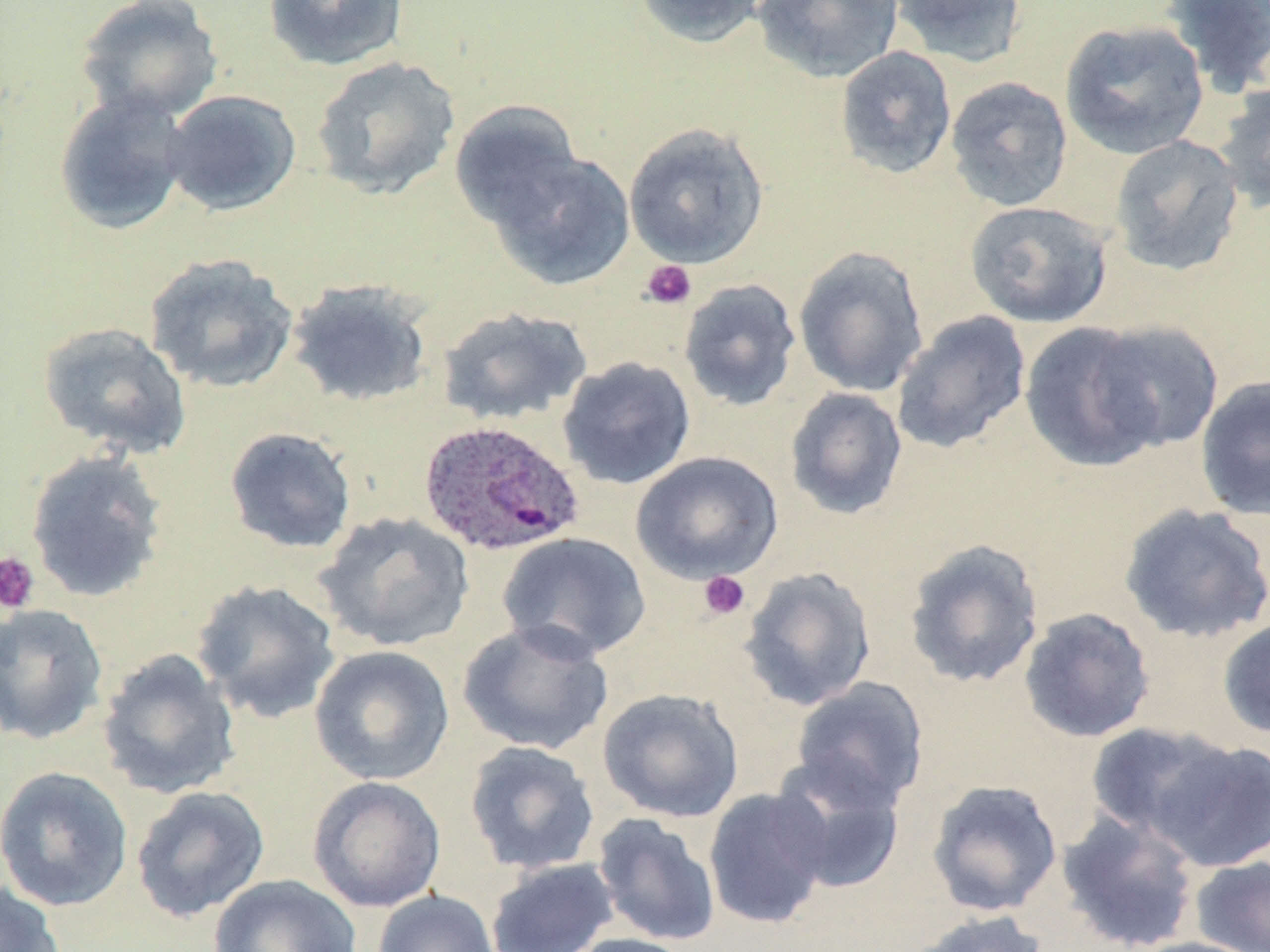
Summary:
  - Coordinate format: approximate bounding boxes as named x1/y1/x2/y2 corners in pixels
  - Uninfected red blood cell locations: (x1=74, y1=0, x2=224, y2=124), (x1=262, y1=0, x2=408, y2=71), (x1=632, y1=0, x2=768, y2=49), (x1=752, y1=0, x2=904, y2=83), (x1=889, y1=0, x2=1028, y2=68), (x1=1161, y1=0, x2=1270, y2=98), (x1=1059, y1=19, x2=1210, y2=160), (x1=834, y1=46, x2=957, y2=179), (x1=311, y1=55, x2=461, y2=200), (x1=944, y1=76, x2=1073, y2=212), (x1=1212, y1=82, x2=1270, y2=214), (x1=161, y1=89, x2=302, y2=216), (x1=53, y1=90, x2=192, y2=236), (x1=448, y1=100, x2=585, y2=233), (x1=623, y1=122, x2=769, y2=268), (x1=1109, y1=135, x2=1246, y2=277), (x1=490, y1=148, x2=636, y2=291), (x1=964, y1=200, x2=1114, y2=328), (x1=793, y1=246, x2=929, y2=397), (x1=143, y1=252, x2=299, y2=395), (x1=286, y1=278, x2=434, y2=408), (x1=678, y1=278, x2=802, y2=412), (x1=436, y1=306, x2=593, y2=425), (x1=890, y1=310, x2=1032, y2=455), (x1=1088, y1=319, x2=1225, y2=453), (x1=37, y1=321, x2=193, y2=459), (x1=1019, y1=321, x2=1165, y2=473), (x1=556, y1=356, x2=696, y2=490), (x1=1195, y1=374, x2=1270, y2=522), (x1=784, y1=387, x2=908, y2=520), (x1=223, y1=426, x2=357, y2=554), (x1=24, y1=449, x2=169, y2=603), (x1=630, y1=451, x2=783, y2=585), (x1=1118, y1=503, x2=1270, y2=644), (x1=314, y1=511, x2=474, y2=652), (x1=496, y1=530, x2=652, y2=661), (x1=902, y1=538, x2=1046, y2=689), (x1=738, y1=566, x2=877, y2=712), (x1=190, y1=580, x2=342, y2=723), (x1=0, y1=603, x2=109, y2=745), (x1=1018, y1=607, x2=1156, y2=743), (x1=1217, y1=615, x2=1270, y2=739), (x1=458, y1=619, x2=613, y2=756), (x1=309, y1=645, x2=455, y2=786), (x1=96, y1=648, x2=241, y2=800), (x1=790, y1=677, x2=929, y2=811), (x1=597, y1=687, x2=745, y2=823), (x1=1084, y1=721, x2=1233, y2=843), (x1=1151, y1=739, x2=1270, y2=872), (x1=464, y1=740, x2=600, y2=875), (x1=768, y1=755, x2=907, y2=895), (x1=0, y1=766, x2=134, y2=912), (x1=307, y1=776, x2=445, y2=913), (x1=926, y1=778, x2=1063, y2=917), (x1=130, y1=785, x2=270, y2=923), (x1=703, y1=787, x2=833, y2=929), (x1=1056, y1=810, x2=1201, y2=951), (x1=592, y1=813, x2=721, y2=946), (x1=1189, y1=856, x2=1270, y2=952), (x1=485, y1=858, x2=620, y2=952), (x1=209, y1=873, x2=364, y2=952), (x1=1, y1=879, x2=65, y2=952), (x1=373, y1=890, x2=501, y2=952), (x1=905, y1=909, x2=1051, y2=952), (x1=561, y1=933, x2=699, y2=952), (x1=1126, y1=936, x2=1267, y2=952)
  - Plasmodium ovale-infected red blood cell locations: (x1=416, y1=419, x2=585, y2=559)
  - Platelet locations: (x1=640, y1=260, x2=697, y2=310), (x1=0, y1=552, x2=40, y2=614), (x1=698, y1=571, x2=750, y2=620)
  - Slide-level diagnosis: Plasmodium ovale
  - Field of view: one of a larger specimen
  - Preparation: thin blood smear
  - Image size: 1270×952 pixels
  - Modality: light microscopy
  - Stain: May-Grünwald-Giemsa
  - Magnification: 1000x